Classify this cell by malaria status.
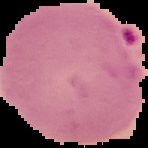

It is parasitized.

Summary:
  - Image size: 148×148 pixels
  - Image type: segmented cell region with the area outside set to black
  - Preparation: thin blood smear